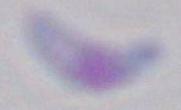

identification = Toxoplasma gondii
magnification = 1000x
modality = micrograph